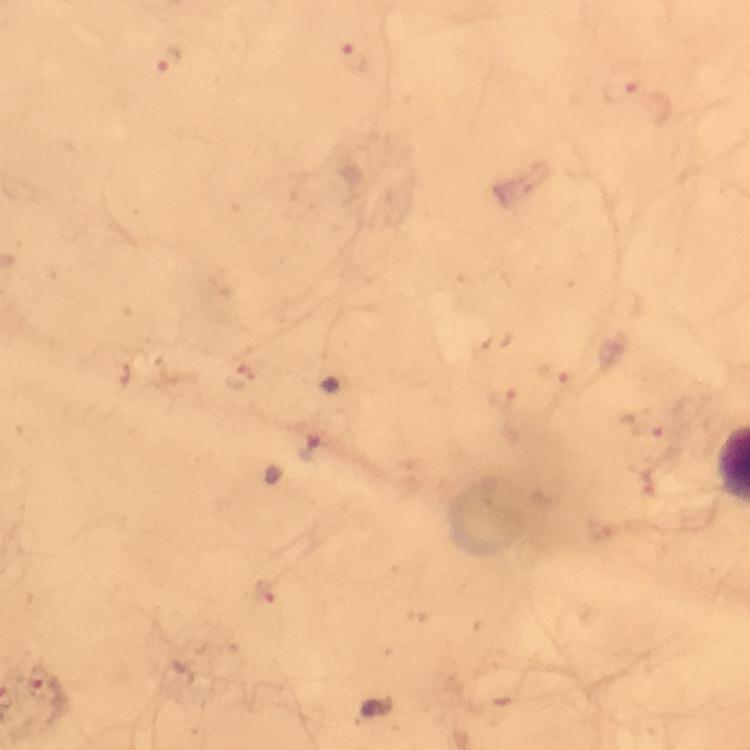

cropped from = one field of view
immersion oil = used
preparation = thick smear
context = from a malaria diagnostic workup
Plasmodium parasite locations = approximate centers as (x, y) in pixels: (354, 56), (169, 59), (623, 89), (564, 377), (238, 378), (503, 399), (649, 423), (264, 588), (43, 685)
magnification = 100x
image size = 750×750 pixels
capture = smartphone mounted on the microscope
stain = Giemsa